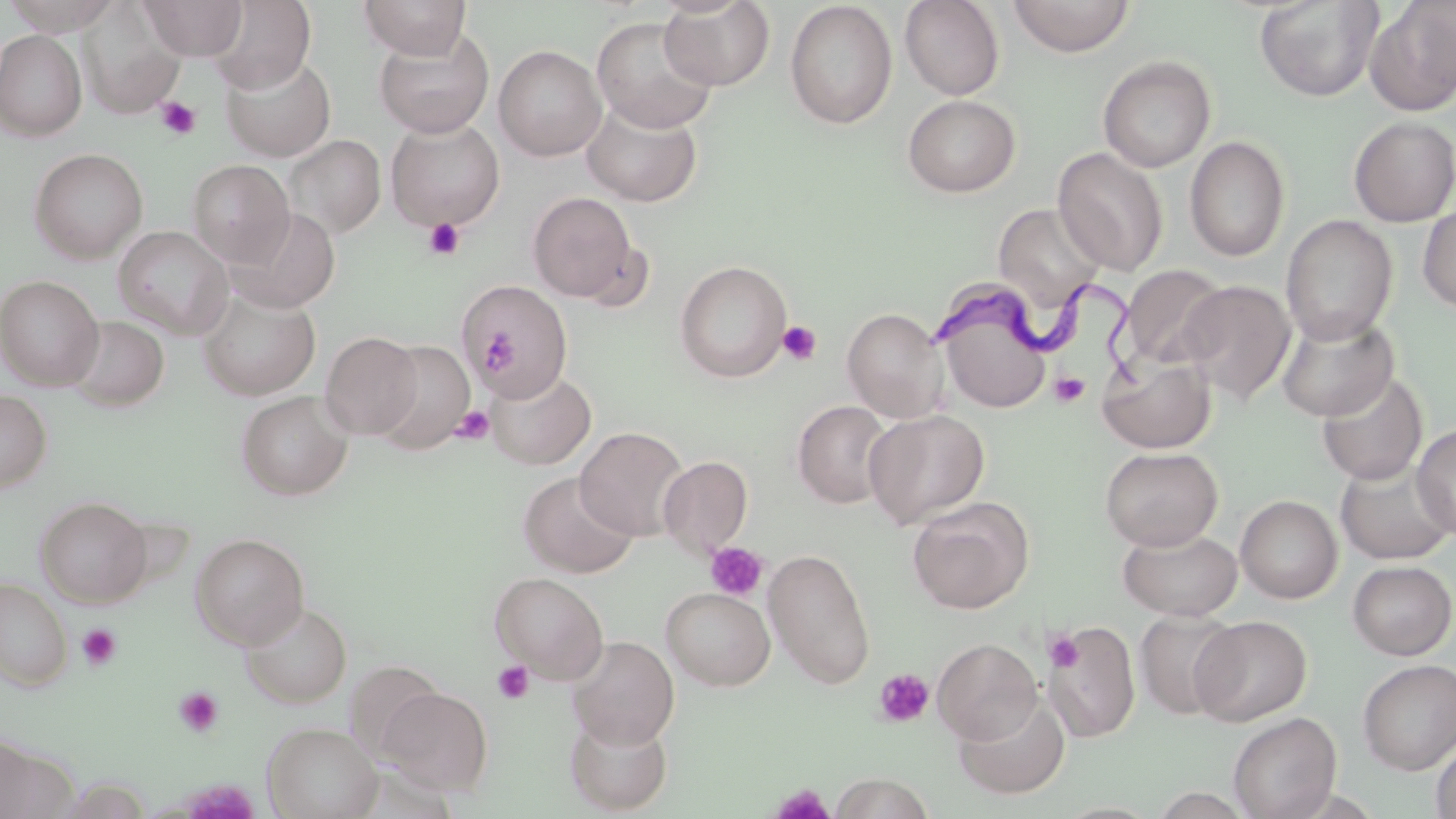
Trypanosoma brucei locations = approximate bounding boxes as named x1/y1/x2/y2 corners in pixels: (x1=936, y1=275, x2=1149, y2=384)
slide-level diagnosis = Trypanosoma brucei
image size = 1456×819 pixels
modality = optical microscopy
platelet locations = approximate bounding boxes as named x1/y1/x2/y2 corners in pixels: (x1=156, y1=97, x2=201, y2=139), (x1=423, y1=217, x2=465, y2=260), (x1=777, y1=320, x2=822, y2=365), (x1=479, y1=328, x2=518, y2=374), (x1=1050, y1=372, x2=1090, y2=406), (x1=451, y1=405, x2=495, y2=445), (x1=705, y1=542, x2=768, y2=601), (x1=77, y1=623, x2=122, y2=672), (x1=1045, y1=629, x2=1084, y2=672), (x1=492, y1=660, x2=535, y2=705), (x1=873, y1=669, x2=935, y2=728), (x1=173, y1=686, x2=225, y2=738), (x1=771, y1=784, x2=835, y2=819)
uninfected red blood cell locations = approximate bounding boxes as named x1/y1/x2/y2 corners in pixels: (x1=2, y1=0, x2=123, y2=35), (x1=140, y1=0, x2=247, y2=60), (x1=209, y1=0, x2=316, y2=93), (x1=358, y1=0, x2=472, y2=59), (x1=659, y1=0, x2=775, y2=91), (x1=899, y1=0, x2=1004, y2=100), (x1=1008, y1=0, x2=1134, y2=57), (x1=784, y1=1, x2=898, y2=129), (x1=1254, y1=1, x2=1384, y2=102), (x1=1365, y1=1, x2=1456, y2=115), (x1=77, y1=3, x2=185, y2=119), (x1=591, y1=16, x2=719, y2=133), (x1=374, y1=27, x2=494, y2=138), (x1=0, y1=29, x2=86, y2=141), (x1=494, y1=45, x2=606, y2=161), (x1=221, y1=53, x2=335, y2=161), (x1=1098, y1=55, x2=1215, y2=173), (x1=902, y1=95, x2=1021, y2=197), (x1=581, y1=98, x2=703, y2=207), (x1=1348, y1=116, x2=1456, y2=227), (x1=385, y1=118, x2=505, y2=231), (x1=283, y1=133, x2=385, y2=239), (x1=1185, y1=135, x2=1290, y2=262), (x1=1053, y1=147, x2=1169, y2=276), (x1=29, y1=148, x2=148, y2=263), (x1=187, y1=159, x2=294, y2=268), (x1=527, y1=192, x2=637, y2=301), (x1=993, y1=202, x2=1107, y2=311), (x1=1417, y1=203, x2=1456, y2=313), (x1=229, y1=207, x2=341, y2=313), (x1=1281, y1=215, x2=1398, y2=344), (x1=113, y1=225, x2=234, y2=339), (x1=675, y1=260, x2=792, y2=383), (x1=1121, y1=264, x2=1229, y2=371), (x1=0, y1=275, x2=103, y2=390), (x1=462, y1=279, x2=575, y2=399), (x1=1178, y1=279, x2=1297, y2=405), (x1=933, y1=283, x2=1053, y2=415), (x1=198, y1=289, x2=320, y2=401), (x1=842, y1=306, x2=950, y2=423), (x1=1277, y1=312, x2=1399, y2=422), (x1=64, y1=315, x2=169, y2=412), (x1=321, y1=331, x2=423, y2=439), (x1=374, y1=340, x2=475, y2=454), (x1=1098, y1=353, x2=1216, y2=453), (x1=485, y1=367, x2=596, y2=470), (x1=1316, y1=371, x2=1428, y2=486), (x1=0, y1=389, x2=52, y2=492), (x1=235, y1=390, x2=353, y2=501), (x1=792, y1=400, x2=895, y2=508), (x1=864, y1=409, x2=990, y2=528), (x1=1412, y1=424, x2=1456, y2=541), (x1=575, y1=426, x2=689, y2=540), (x1=1101, y1=446, x2=1223, y2=550), (x1=658, y1=455, x2=753, y2=557), (x1=1336, y1=460, x2=1455, y2=566), (x1=519, y1=472, x2=638, y2=578), (x1=907, y1=495, x2=1034, y2=614), (x1=1235, y1=495, x2=1342, y2=603), (x1=35, y1=496, x2=152, y2=607), (x1=1118, y1=527, x2=1242, y2=620), (x1=190, y1=533, x2=309, y2=650), (x1=763, y1=548, x2=876, y2=689), (x1=1348, y1=560, x2=1456, y2=660), (x1=490, y1=571, x2=608, y2=683), (x1=0, y1=580, x2=72, y2=690), (x1=661, y1=587, x2=775, y2=690), (x1=241, y1=601, x2=351, y2=707), (x1=1134, y1=609, x2=1242, y2=720), (x1=1191, y1=615, x2=1312, y2=726), (x1=1042, y1=623, x2=1140, y2=741), (x1=566, y1=635, x2=680, y2=748), (x1=932, y1=638, x2=1043, y2=744), (x1=1357, y1=659, x2=1456, y2=775), (x1=378, y1=687, x2=493, y2=795), (x1=954, y1=693, x2=1070, y2=799), (x1=565, y1=711, x2=674, y2=815), (x1=1229, y1=712, x2=1341, y2=819), (x1=263, y1=722, x2=381, y2=819), (x1=1430, y1=738, x2=1456, y2=819), (x1=1, y1=740, x2=73, y2=818), (x1=828, y1=773, x2=936, y2=818)
field of view = single
stain = May-Grünwald-Giemsa
preparation = thin blood smear
magnification = 1000x